State which cell type is depicted.
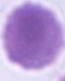
This is an erythrocyte.

Captured at 1000x magnification. Micrograph.